Assess this cell for malaria.
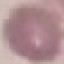
Uninfected.

Summary:
  - Preparation: thin blood film
  - Stain: Giemsa
  - Capture: smartphone camera at the microscope eyepiece
  - Image type: automatically extracted cell patch, resized to 64 × 64 pixels